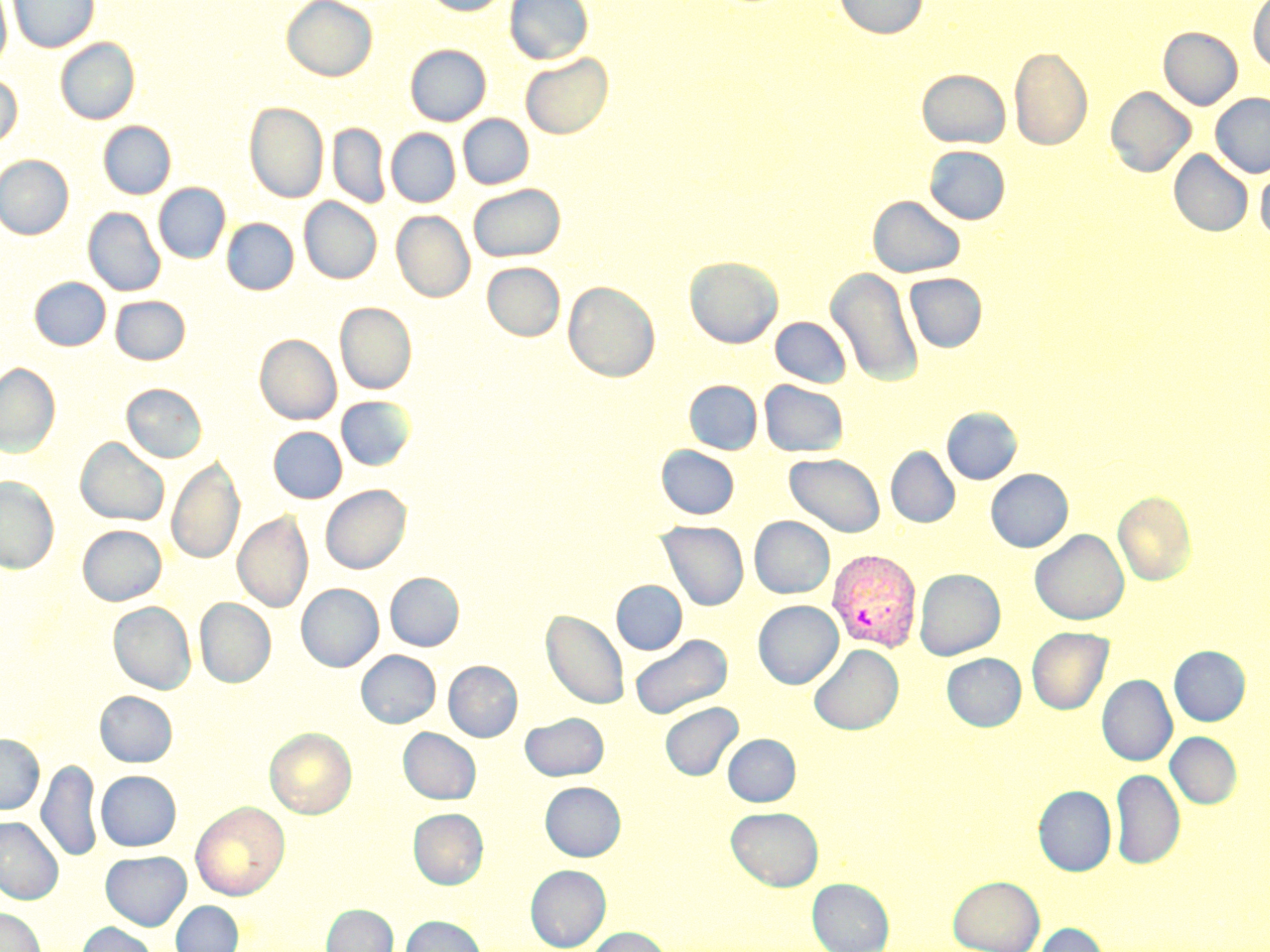

Approximate bounding boxes as named x1/y1/x2/y2 corners in pixels. Uninfected red blood cell locations: (x1=0, y1=0, x2=11, y2=73), (x1=8, y1=0, x2=99, y2=52), (x1=282, y1=0, x2=377, y2=81), (x1=423, y1=0, x2=511, y2=16), (x1=505, y1=0, x2=592, y2=64), (x1=834, y1=0, x2=928, y2=39), (x1=1248, y1=0, x2=1270, y2=71), (x1=1159, y1=27, x2=1242, y2=110), (x1=56, y1=37, x2=139, y2=124), (x1=406, y1=44, x2=490, y2=125), (x1=1009, y1=46, x2=1092, y2=150), (x1=521, y1=53, x2=613, y2=138), (x1=917, y1=69, x2=1010, y2=148), (x1=0, y1=72, x2=22, y2=148), (x1=1105, y1=86, x2=1195, y2=178), (x1=1211, y1=93, x2=1270, y2=178), (x1=245, y1=102, x2=328, y2=203), (x1=458, y1=114, x2=533, y2=188), (x1=99, y1=121, x2=175, y2=199), (x1=328, y1=123, x2=390, y2=208), (x1=386, y1=128, x2=460, y2=207), (x1=924, y1=146, x2=1011, y2=224), (x1=1169, y1=150, x2=1253, y2=237), (x1=0, y1=155, x2=73, y2=240), (x1=1256, y1=163, x2=1270, y2=244), (x1=154, y1=183, x2=230, y2=263), (x1=469, y1=184, x2=565, y2=261), (x1=868, y1=195, x2=966, y2=278), (x1=299, y1=197, x2=382, y2=283), (x1=83, y1=207, x2=165, y2=296), (x1=392, y1=210, x2=474, y2=302), (x1=222, y1=218, x2=298, y2=295), (x1=685, y1=256, x2=782, y2=348), (x1=482, y1=262, x2=565, y2=340), (x1=826, y1=268, x2=923, y2=387), (x1=904, y1=273, x2=986, y2=352), (x1=30, y1=277, x2=111, y2=350), (x1=563, y1=281, x2=660, y2=382), (x1=110, y1=296, x2=190, y2=364), (x1=335, y1=302, x2=416, y2=394), (x1=771, y1=317, x2=851, y2=387), (x1=255, y1=334, x2=341, y2=424), (x1=0, y1=363, x2=60, y2=456), (x1=685, y1=380, x2=762, y2=454), (x1=759, y1=380, x2=848, y2=456), (x1=122, y1=383, x2=207, y2=462), (x1=336, y1=396, x2=414, y2=470), (x1=942, y1=408, x2=1021, y2=484), (x1=269, y1=426, x2=346, y2=503), (x1=76, y1=438, x2=169, y2=526), (x1=656, y1=445, x2=740, y2=519), (x1=886, y1=447, x2=960, y2=528), (x1=785, y1=453, x2=885, y2=537), (x1=168, y1=456, x2=244, y2=565), (x1=986, y1=469, x2=1073, y2=552), (x1=0, y1=476, x2=59, y2=573), (x1=321, y1=485, x2=410, y2=574), (x1=1113, y1=491, x2=1196, y2=586), (x1=234, y1=511, x2=313, y2=612), (x1=749, y1=516, x2=835, y2=599), (x1=656, y1=521, x2=750, y2=610), (x1=78, y1=525, x2=166, y2=605), (x1=1030, y1=529, x2=1129, y2=625), (x1=915, y1=568, x2=1005, y2=660), (x1=385, y1=572, x2=464, y2=651), (x1=612, y1=580, x2=687, y2=654), (x1=297, y1=584, x2=383, y2=672), (x1=195, y1=598, x2=275, y2=687), (x1=753, y1=600, x2=843, y2=689), (x1=108, y1=601, x2=196, y2=694), (x1=542, y1=609, x2=629, y2=709), (x1=1027, y1=627, x2=1113, y2=714), (x1=629, y1=634, x2=732, y2=719), (x1=809, y1=644, x2=903, y2=735), (x1=1169, y1=646, x2=1250, y2=726), (x1=357, y1=650, x2=440, y2=728), (x1=942, y1=653, x2=1026, y2=731), (x1=444, y1=661, x2=522, y2=741), (x1=1097, y1=675, x2=1177, y2=766), (x1=95, y1=691, x2=177, y2=767), (x1=660, y1=702, x2=743, y2=780), (x1=520, y1=713, x2=609, y2=780), (x1=265, y1=728, x2=356, y2=818), (x1=399, y1=728, x2=480, y2=804), (x1=1166, y1=732, x2=1242, y2=809), (x1=0, y1=734, x2=44, y2=814), (x1=723, y1=734, x2=800, y2=806), (x1=37, y1=759, x2=102, y2=862), (x1=1110, y1=768, x2=1185, y2=870), (x1=96, y1=771, x2=181, y2=851), (x1=540, y1=782, x2=625, y2=861), (x1=1034, y1=785, x2=1116, y2=876), (x1=191, y1=801, x2=290, y2=900), (x1=726, y1=806, x2=823, y2=891), (x1=409, y1=808, x2=488, y2=889), (x1=0, y1=817, x2=63, y2=904), (x1=100, y1=851, x2=191, y2=930), (x1=526, y1=865, x2=610, y2=950), (x1=948, y1=875, x2=1044, y2=952), (x1=808, y1=878, x2=894, y2=952), (x1=171, y1=901, x2=243, y2=952), (x1=322, y1=904, x2=397, y2=952), (x1=0, y1=908, x2=45, y2=952), (x1=400, y1=916, x2=486, y2=952), (x1=77, y1=922, x2=157, y2=952), (x1=1032, y1=923, x2=1109, y2=952), (x1=585, y1=927, x2=671, y2=952). Plasmodium vivax-infected red blood cell locations: (x1=826, y1=548, x2=923, y2=653). Slide-level diagnosis: Plasmodium vivax. Thin blood smear. Captured at 1000x magnification. Light microscopy. May-Grünwald-Giemsa-stained preparation. One field of a larger specimen. Image is 1270×952 pixels.